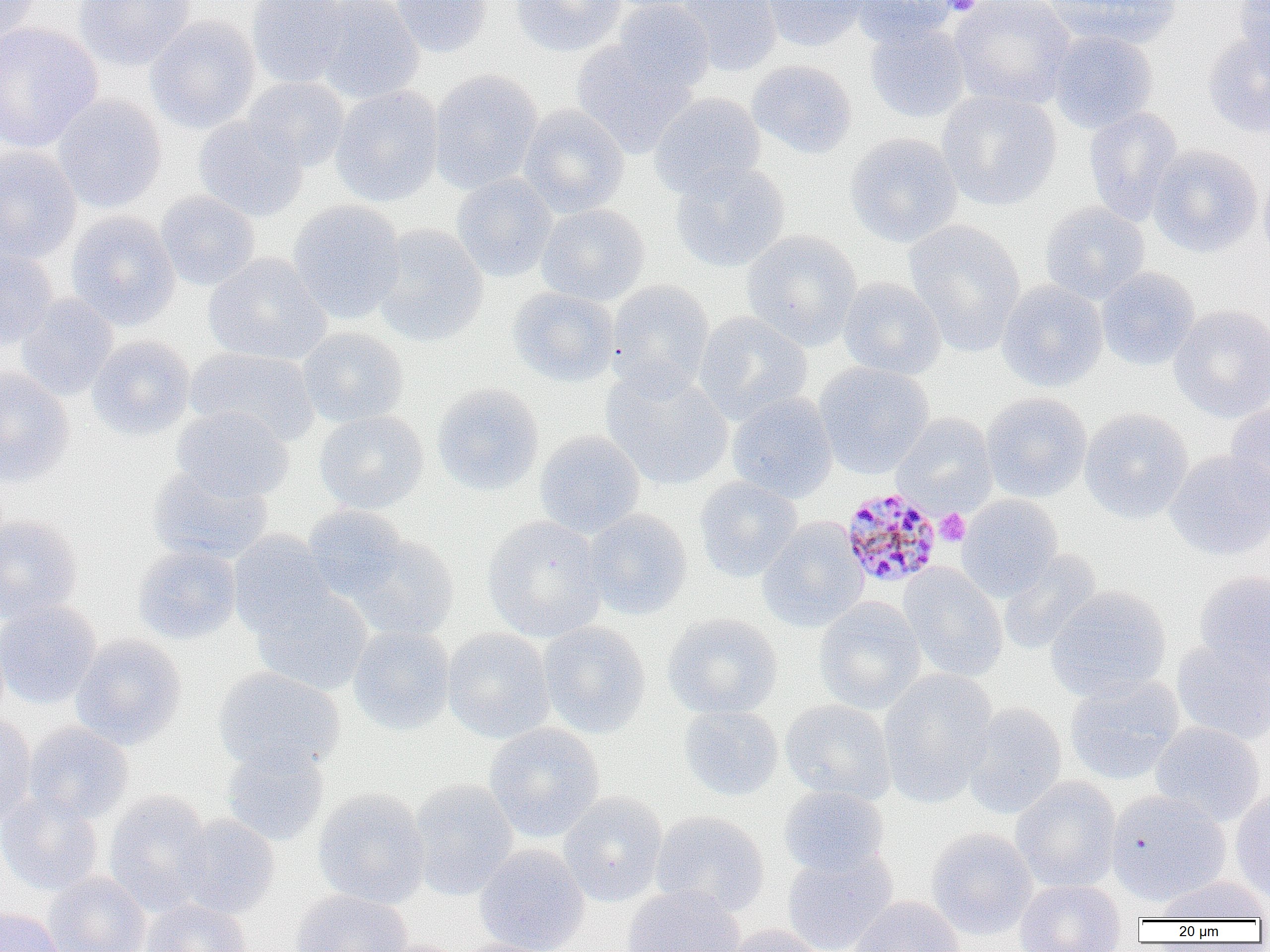
Summary:
  - Coordinate format: approximate bounding boxes as named x1/y1/x2/y2 corners in pixels
  - Plasmodium malariae-infected red blood cell locations: (x1=840, y1=486, x2=944, y2=589)
  - Platelet locations: (x1=939, y1=0, x2=985, y2=16), (x1=935, y1=509, x2=970, y2=546)
  - Uninfected red blood cell locations: (x1=0, y1=0, x2=40, y2=42), (x1=73, y1=0, x2=196, y2=71), (x1=247, y1=0, x2=350, y2=88), (x1=313, y1=0, x2=424, y2=103), (x1=391, y1=0, x2=492, y2=57), (x1=511, y1=0, x2=627, y2=57), (x1=600, y1=0, x2=712, y2=13), (x1=612, y1=0, x2=714, y2=95), (x1=676, y1=0, x2=782, y2=77), (x1=762, y1=0, x2=868, y2=52), (x1=848, y1=0, x2=959, y2=47), (x1=948, y1=0, x2=1077, y2=111), (x1=1044, y1=0, x2=1182, y2=49), (x1=1234, y1=0, x2=1270, y2=67), (x1=145, y1=15, x2=261, y2=134), (x1=864, y1=21, x2=971, y2=123), (x1=0, y1=22, x2=103, y2=154), (x1=1049, y1=30, x2=1158, y2=133), (x1=1204, y1=32, x2=1270, y2=137), (x1=571, y1=40, x2=695, y2=158), (x1=746, y1=59, x2=857, y2=158), (x1=428, y1=69, x2=543, y2=194), (x1=243, y1=76, x2=349, y2=172), (x1=330, y1=85, x2=444, y2=207), (x1=937, y1=89, x2=1061, y2=211), (x1=649, y1=92, x2=767, y2=199), (x1=51, y1=95, x2=167, y2=213), (x1=518, y1=105, x2=629, y2=218), (x1=1083, y1=107, x2=1183, y2=226), (x1=193, y1=115, x2=309, y2=222), (x1=844, y1=132, x2=963, y2=248), (x1=1148, y1=144, x2=1263, y2=258), (x1=0, y1=145, x2=82, y2=263), (x1=669, y1=162, x2=790, y2=272), (x1=1259, y1=167, x2=1270, y2=268), (x1=451, y1=173, x2=558, y2=282), (x1=155, y1=191, x2=261, y2=291), (x1=288, y1=200, x2=406, y2=323), (x1=1040, y1=203, x2=1150, y2=304), (x1=537, y1=204, x2=650, y2=306), (x1=65, y1=211, x2=181, y2=331), (x1=903, y1=220, x2=1027, y2=355), (x1=372, y1=225, x2=489, y2=347), (x1=741, y1=229, x2=862, y2=350), (x1=0, y1=247, x2=57, y2=351), (x1=203, y1=253, x2=331, y2=366), (x1=1095, y1=267, x2=1200, y2=371), (x1=837, y1=276, x2=946, y2=380), (x1=606, y1=280, x2=715, y2=396), (x1=996, y1=280, x2=1108, y2=392), (x1=508, y1=287, x2=621, y2=387), (x1=16, y1=294, x2=119, y2=401), (x1=1169, y1=304, x2=1270, y2=422), (x1=693, y1=311, x2=812, y2=425), (x1=297, y1=326, x2=408, y2=427), (x1=86, y1=336, x2=195, y2=441), (x1=185, y1=347, x2=321, y2=447), (x1=813, y1=362, x2=934, y2=478), (x1=601, y1=366, x2=733, y2=491), (x1=0, y1=367, x2=75, y2=486), (x1=431, y1=382, x2=544, y2=497), (x1=726, y1=392, x2=838, y2=503), (x1=980, y1=392, x2=1092, y2=503), (x1=1225, y1=400, x2=1270, y2=508), (x1=171, y1=406, x2=294, y2=503), (x1=1080, y1=408, x2=1194, y2=523), (x1=314, y1=410, x2=429, y2=513), (x1=891, y1=413, x2=998, y2=515), (x1=534, y1=430, x2=646, y2=538), (x1=1164, y1=449, x2=1270, y2=561), (x1=148, y1=465, x2=273, y2=564), (x1=694, y1=477, x2=803, y2=583), (x1=957, y1=494, x2=1063, y2=600), (x1=302, y1=505, x2=411, y2=602), (x1=583, y1=509, x2=692, y2=621), (x1=0, y1=514, x2=83, y2=623), (x1=482, y1=515, x2=608, y2=642), (x1=757, y1=517, x2=869, y2=633), (x1=227, y1=531, x2=335, y2=638), (x1=345, y1=533, x2=459, y2=641), (x1=133, y1=544, x2=242, y2=645), (x1=998, y1=549, x2=1102, y2=656), (x1=898, y1=563, x2=1008, y2=682), (x1=1193, y1=571, x2=1270, y2=682), (x1=1044, y1=585, x2=1172, y2=702), (x1=251, y1=587, x2=373, y2=695), (x1=814, y1=597, x2=926, y2=715), (x1=0, y1=601, x2=101, y2=709), (x1=663, y1=613, x2=783, y2=719), (x1=538, y1=621, x2=651, y2=738), (x1=348, y1=625, x2=455, y2=735), (x1=441, y1=628, x2=556, y2=744), (x1=70, y1=634, x2=187, y2=749), (x1=1171, y1=640, x2=1270, y2=745), (x1=213, y1=667, x2=345, y2=776), (x1=878, y1=669, x2=998, y2=806), (x1=1065, y1=674, x2=1185, y2=784), (x1=780, y1=698, x2=896, y2=805), (x1=962, y1=702, x2=1067, y2=819), (x1=678, y1=705, x2=783, y2=801), (x1=0, y1=711, x2=37, y2=827), (x1=1150, y1=721, x2=1265, y2=827), (x1=23, y1=722, x2=133, y2=824), (x1=484, y1=722, x2=605, y2=842), (x1=221, y1=743, x2=330, y2=846), (x1=1011, y1=776, x2=1121, y2=893), (x1=409, y1=778, x2=519, y2=900), (x1=778, y1=785, x2=890, y2=878), (x1=1230, y1=787, x2=1270, y2=904), (x1=312, y1=789, x2=431, y2=909), (x1=104, y1=790, x2=214, y2=913), (x1=1106, y1=790, x2=1231, y2=906), (x1=559, y1=791, x2=668, y2=907), (x1=0, y1=792, x2=103, y2=896), (x1=649, y1=811, x2=770, y2=918), (x1=172, y1=815, x2=280, y2=919), (x1=926, y1=828, x2=1037, y2=940), (x1=474, y1=844, x2=590, y2=952), (x1=782, y1=848, x2=898, y2=952), (x1=42, y1=872, x2=151, y2=952), (x1=1153, y1=875, x2=1270, y2=922), (x1=1014, y1=879, x2=1126, y2=952), (x1=621, y1=884, x2=745, y2=952), (x1=291, y1=889, x2=412, y2=952), (x1=847, y1=896, x2=966, y2=952), (x1=140, y1=898, x2=252, y2=952), (x1=1, y1=906, x2=64, y2=952), (x1=721, y1=925, x2=828, y2=952), (x1=453, y1=939, x2=564, y2=952)
  - Slide-level diagnosis: Plasmodium malariae
  - Preparation: thin blood smear
  - Field of view: one of a larger specimen
  - Image size: 1270×952 pixels
  - Magnification: 1000x
  - Modality: light microscopy